Identify the preparation type.
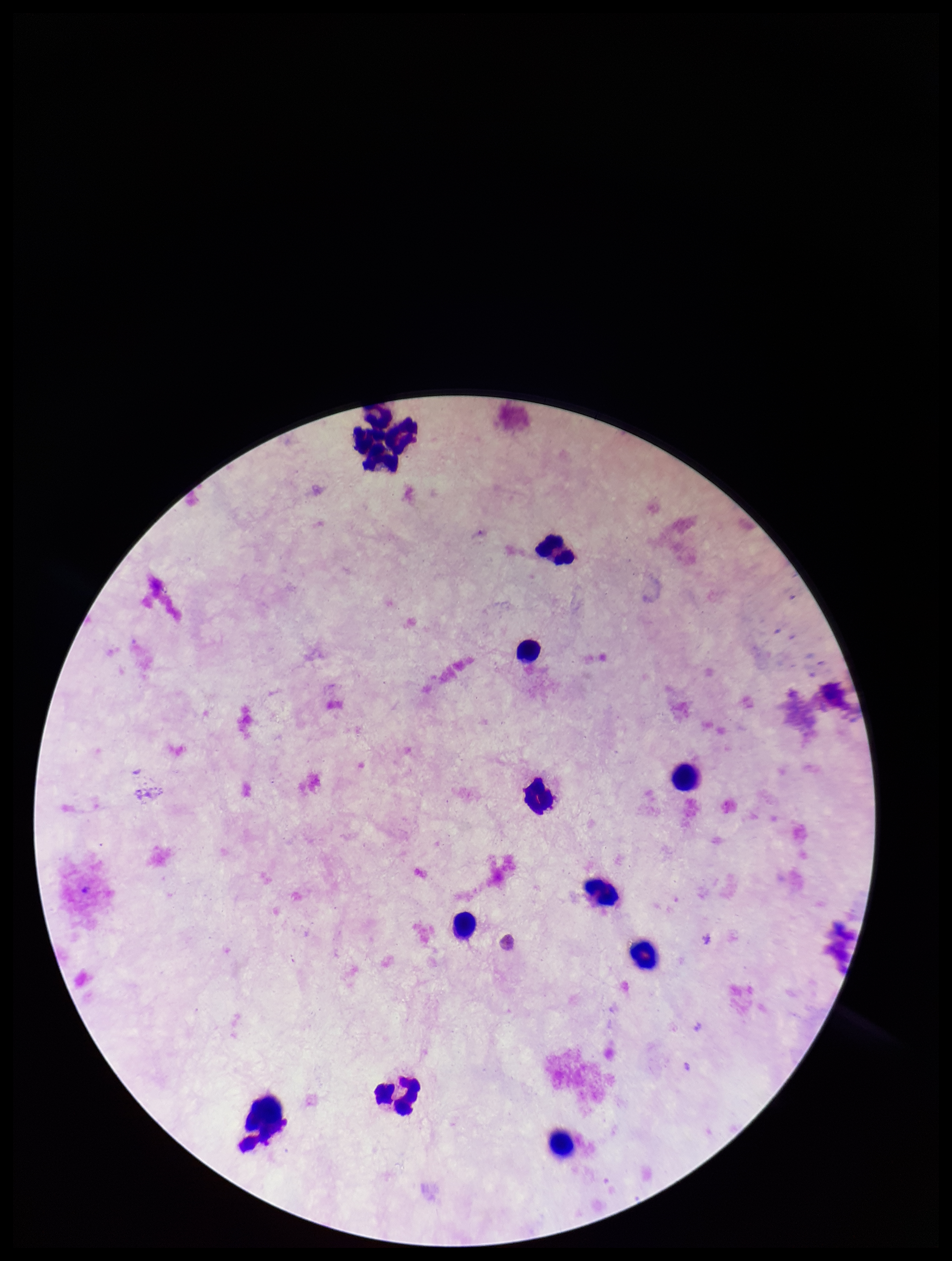
It is a thick blood smear.

Summary:
  - Capture: smartphone photograph through the microscope eyepiece
  - Leukocyte count: 12
  - Image size: 952×1261 pixels
  - Field of view: single
  - Stain: Giemsa
  - Patient malaria status: negative
  - Parasite count: 0
  - Plasmodium parasites: none detected